State the blood parasite species.
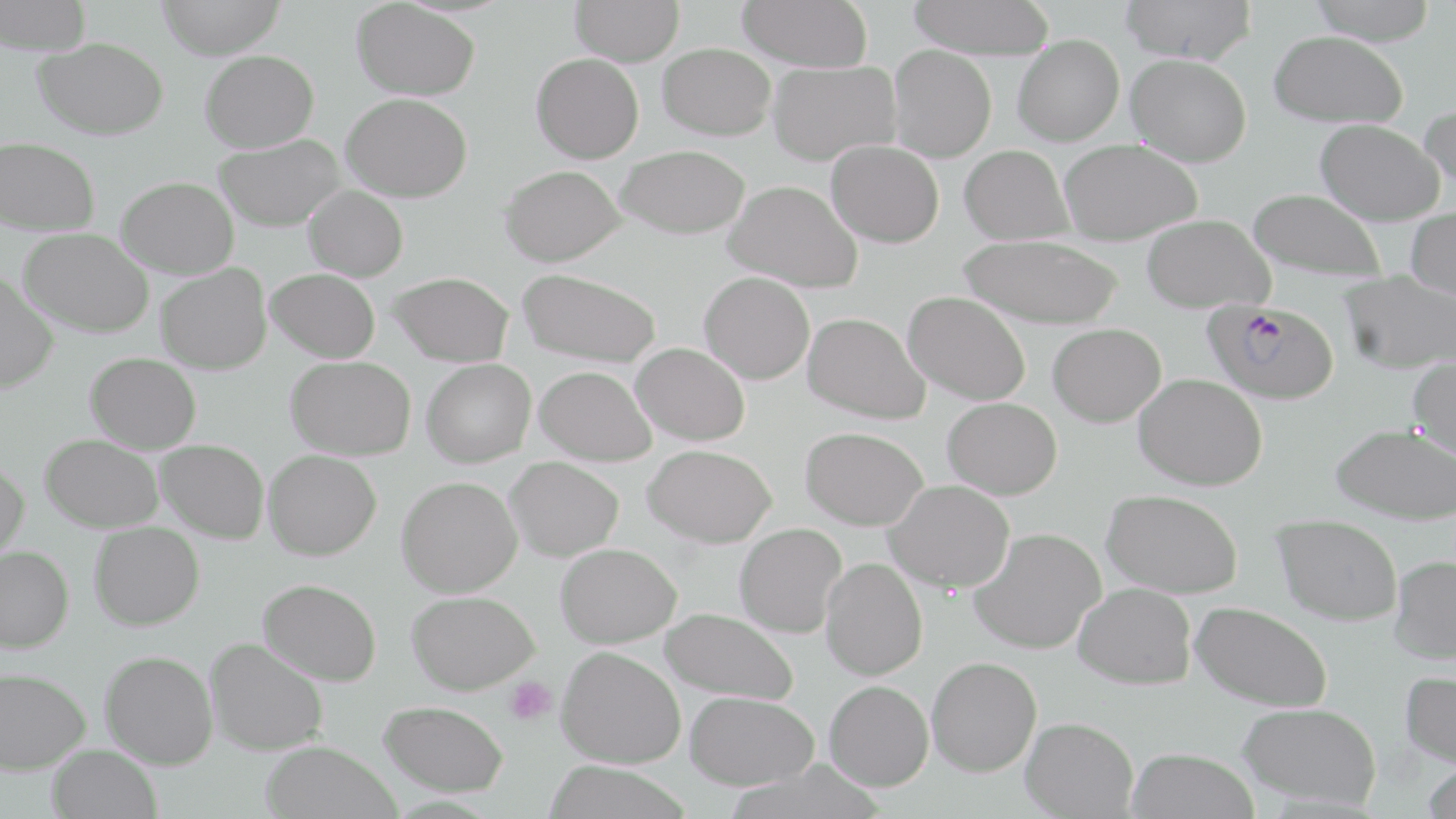

Plasmodium falciparum.

Approximate bounding boxes as (x1,y1)-(x2,y2) corner pairs in pixels. Uninfected red blood cell locations: (0,0)-(92,56), (156,0)-(286,59), (570,0)-(684,66), (737,0)-(873,72), (907,0)-(1055,59), (1119,0)-(1258,64), (1307,0)-(1438,44), (352,1)-(480,100), (1268,30)-(1408,128), (1013,34)-(1124,145), (35,38)-(171,139), (658,43)-(776,140), (889,45)-(997,161), (201,50)-(319,152), (531,53)-(644,163), (1126,54)-(1251,166), (768,60)-(900,165), (342,93)-(472,202), (1419,100)-(1456,203), (1315,119)-(1444,225), (214,134)-(346,231), (0,137)-(100,235), (826,140)-(944,247), (1060,140)-(1202,244), (616,145)-(752,238), (960,145)-(1073,245), (500,165)-(625,266), (116,177)-(239,277), (723,179)-(863,292), (304,185)-(408,281), (1248,187)-(1387,283), (1406,206)-(1456,301), (1141,214)-(1274,313), (19,228)-(153,337), (958,234)-(1125,329), (156,264)-(271,374), (266,268)-(380,362), (518,268)-(662,368), (1339,270)-(1455,374), (0,271)-(58,393), (388,271)-(514,367), (700,272)-(815,384), (903,291)-(1031,405), (804,312)-(931,423), (1048,323)-(1166,427), (631,342)-(750,446), (86,352)-(201,453), (287,356)-(416,459), (1408,356)-(1456,460), (422,359)-(535,467), (534,365)-(657,466), (1134,373)-(1267,490), (942,397)-(1062,499), (1331,424)-(1456,524), (801,426)-(928,530), (41,434)-(164,531), (156,439)-(269,543), (643,444)-(777,547), (264,449)-(381,560), (505,456)-(623,561), (0,460)-(29,564), (397,476)-(522,597), (884,480)-(1014,592), (1102,489)-(1243,597), (1273,514)-(1403,625), (89,522)-(204,630), (735,523)-(845,638), (970,528)-(1105,653), (555,543)-(681,648), (0,545)-(74,652), (1389,555)-(1456,663), (821,557)-(928,680), (258,578)-(382,686), (1074,583)-(1196,689), (407,591)-(540,694), (1190,602)-(1333,711), (660,607)-(799,704), (205,637)-(328,755), (556,646)-(686,768), (100,650)-(218,769), (926,656)-(1041,776), (0,667)-(90,773), (1399,670)-(1456,769), (824,680)-(933,791), (684,691)-(819,789), (379,700)-(509,796), (1238,703)-(1381,808), (1020,717)-(1138,818), (260,740)-(401,819), (47,745)-(162,819), (1127,747)-(1259,819), (542,761)-(692,819), (1420,763)-(1456,818). Platelet locations: (504,676)-(558,724). Plasmodium falciparum-infected red blood cell locations: (1203,298)-(1340,405). Optical microscopy. Single field of view. Captured at 1000x magnification. May-Grünwald-Giemsa stain. Image is 1456×819 pixels. Thin blood smear.